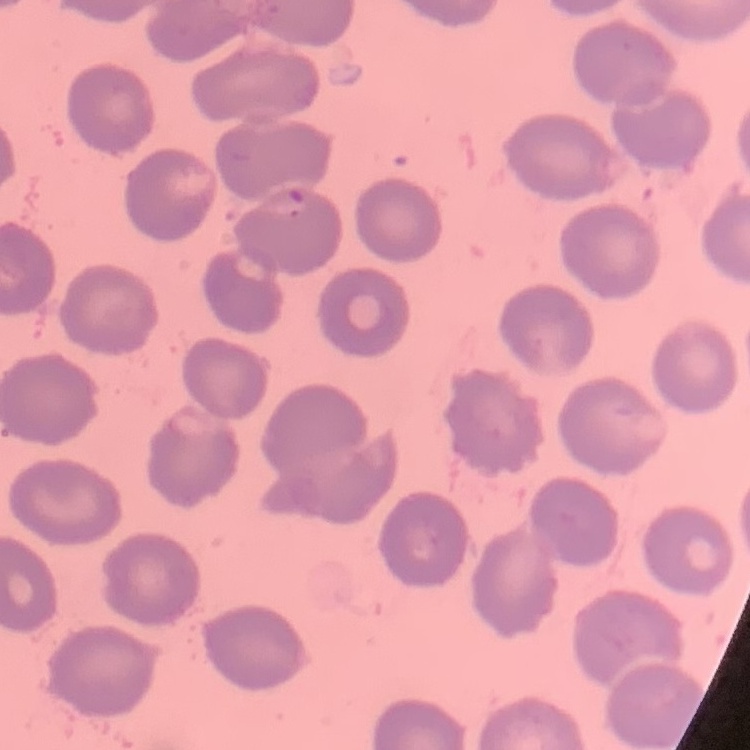

red_blood_cell_morphology: no rouleaux formation
image_type: square crop of a larger photomicrograph
stain: Field's or Giemsa
preparation: thin blood smear